Outline each blood parasite and name the species.
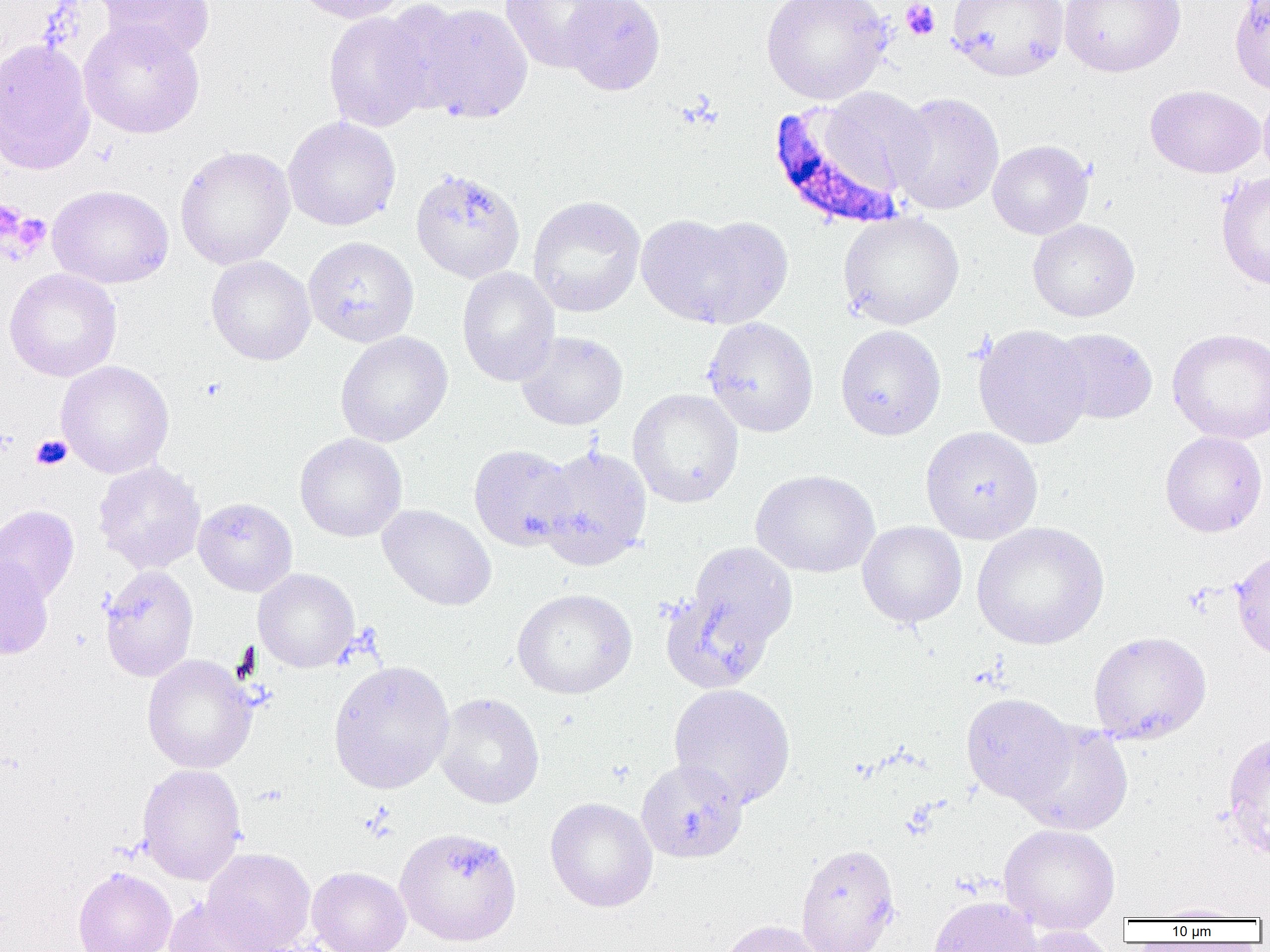

Approximate bounding boxes as (x1,y1)-(x2,y2) corner pairs in pixels.
Plasmodium falciparum-infected red blood cells: (767,103)-(907,231).
No Plasmodium ovale, Plasmodium malariae, Plasmodium vivax, Babesia divergens, or Trypanosoma brucei observed.

Summary:
  - Uninfected red blood cell locations: (95,0)-(215,61), (289,0)-(410,24), (499,0)-(623,73), (561,0)-(665,95), (760,0)-(892,104), (947,0)-(1068,81), (1059,0)-(1186,77), (1229,0)-(1270,95), (413,3)-(533,124), (323,11)-(433,132), (78,20)-(206,139), (0,38)-(96,176), (1145,85)-(1265,178), (818,87)-(932,194), (1258,87)-(1270,182), (889,92)-(1004,215), (282,116)-(401,231), (987,140)-(1093,239), (174,145)-(296,270), (410,168)-(526,283), (1216,172)-(1270,290), (48,184)-(173,289), (527,195)-(646,317), (837,212)-(965,330), (638,214)-(792,329), (1027,219)-(1140,322), (304,236)-(419,347), (206,255)-(316,365), (456,267)-(560,387), (3,268)-(122,382), (702,317)-(819,437), (972,324)-(1093,449), (835,325)-(946,440), (1049,328)-(1158,424), (1167,328)-(1270,444), (515,330)-(628,431), (335,331)-(453,447), (55,360)-(174,478), (627,388)-(744,508), (920,426)-(1043,544), (1160,431)-(1268,537), (294,433)-(407,542), (469,444)-(576,551), (535,445)-(653,569), (93,459)-(206,574), (751,469)-(880,578), (193,497)-(297,596), (377,504)-(497,611), (0,505)-(79,604), (857,521)-(967,628), (972,521)-(1109,650), (685,542)-(798,652), (1231,550)-(1270,660), (0,556)-(53,659), (99,565)-(199,681), (253,568)-(359,672), (512,588)-(637,699), (659,588)-(778,693), (1088,631)-(1211,744), (142,654)-(256,774), (328,660)-(455,794), (667,683)-(796,809), (960,692)-(1078,805), (435,693)-(545,809), (1014,722)-(1135,835), (1222,731)-(1270,862), (636,759)-(748,863), (137,763)-(247,885), (545,797)-(658,912), (999,824)-(1120,935), (795,843)-(900,952), (202,847)-(315,952), (73,866)-(176,952), (306,866)-(411,952), (164,895)-(270,952), (928,896)-(1043,952), (1146,903)-(1256,921), (718,919)-(828,952), (1013,926)-(1119,952)
  - Platelet locations: (900,0)-(940,41), (0,200)-(26,241), (4,212)-(52,258), (31,435)-(72,471)
  - Slide-level diagnosis: Plasmodium falciparum
  - Image size: 1270×952 pixels
  - Field of view: one of a larger specimen
  - Magnification: 1000x
  - Preparation: thin blood smear
  - Modality: optical microscopy